Assess the morphology of the erythrocytes.
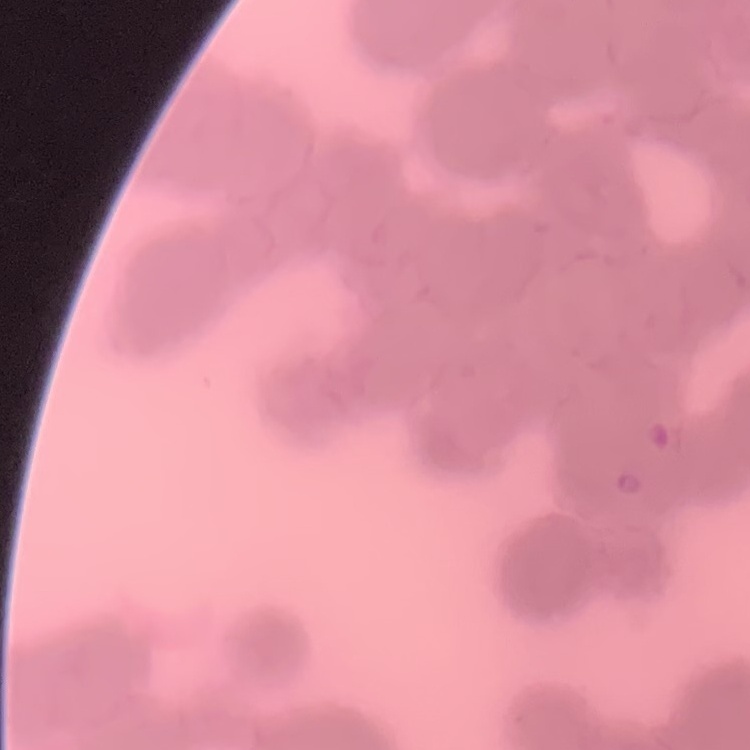
They show rouleaux formation.

Summary:
  - Preparation: thin blood film
  - Image type: one tile cut from a larger photomicrograph
  - Stain: Field's or Giemsa